Classify this cell by malaria status.
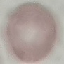

Uninfected.

preparation = thin blood smear
capture = smartphone camera at the microscope eyepiece
stain = Giemsa
image type = cell patch, automatically extracted from a larger field of view and resized to 64 × 64 pixels